Classify this cell by malaria status.
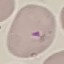
Parasitized.

Cell patch, automatically extracted from a larger field of view and resized to 64 × 64 pixels. Photographed with a smartphone camera at the microscope eyepiece. Thin blood smear. Giemsa stain.